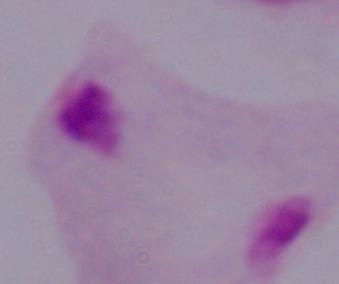
{
  "identification": "trichomonad",
  "magnification": "1000x",
  "modality": "photomicrograph"
}